Comment on the morphology of the erythrocytes.
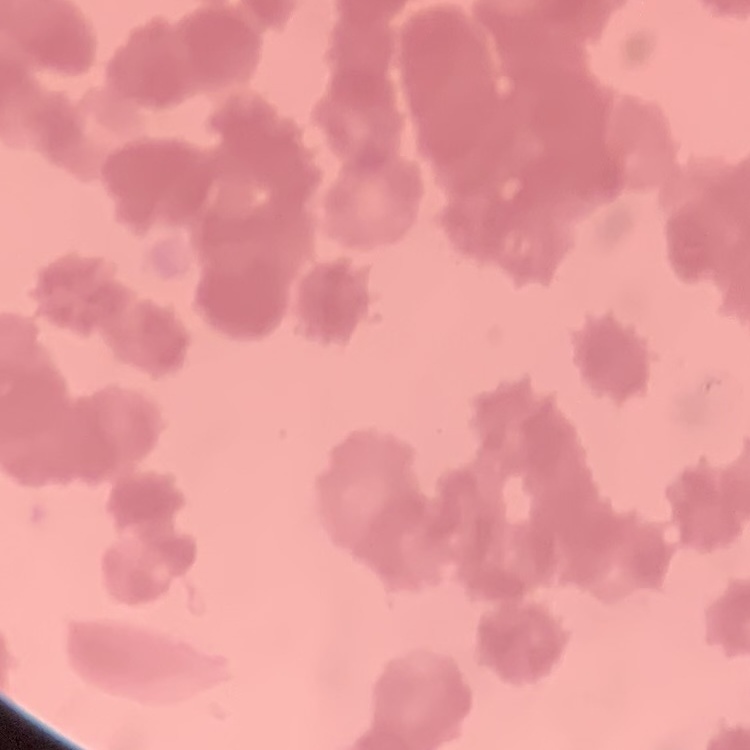

They show rouleaux formation.

Thin blood film. Square crop of a larger photomicrograph. Stained with either Field's or Giemsa.